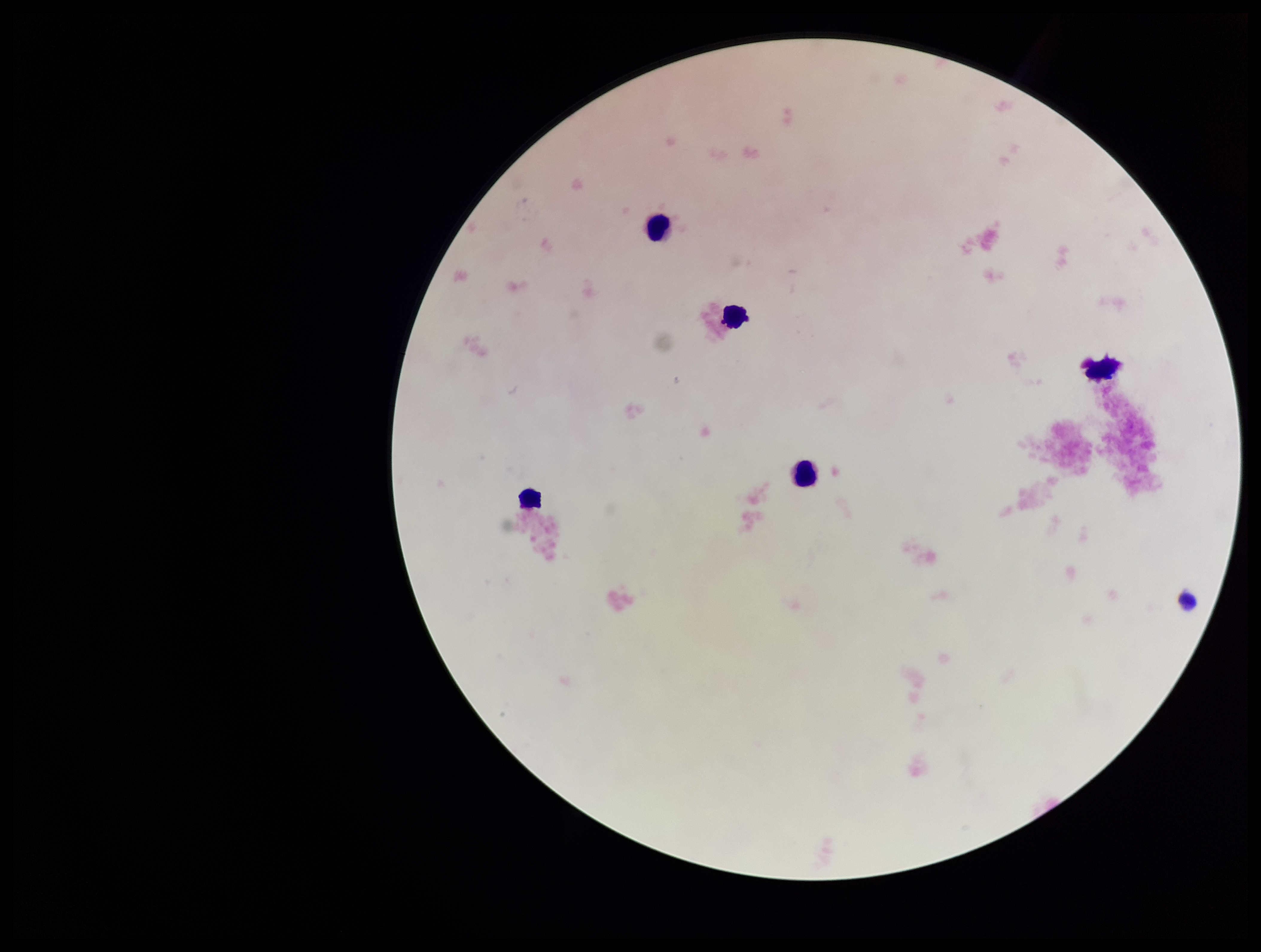
stain: Giemsa
leukocyte_count: 5
capture: smartphone photograph through the microscope eyepiece
parasite_count: 0
image_size: 1261×952 pixels
plasmodium_parasites: none seen
patient_malaria_status: negative
preparation: thick blood smear
field_of_view: one from this slide